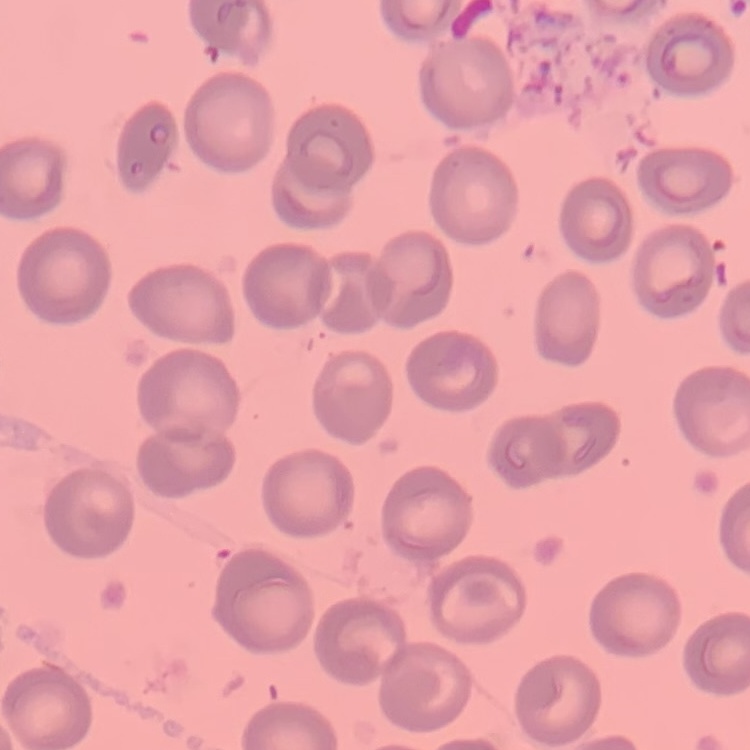

{
  "erythrocyte_morphology": "no rouleaux formation",
  "preparation": "thin blood film",
  "image_type": "one tile cut from a larger photomicrograph",
  "stain": "Field's or Giemsa"
}